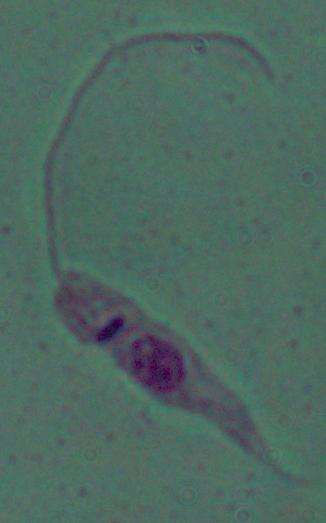

{
  "identification": "Leishmania",
  "magnification": "1000x",
  "modality": "photomicrograph"
}